Assess this cell for malaria.
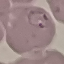
Parasitized.

Summary:
  - Capture: smartphone camera at the microscope eyepiece
  - Preparation: thin blood film
  - Image type: cell patch, automatically extracted from a larger field of view and resized to 64 × 64 pixels
  - Stain: Giemsa